Look for Plasmodium parasites.
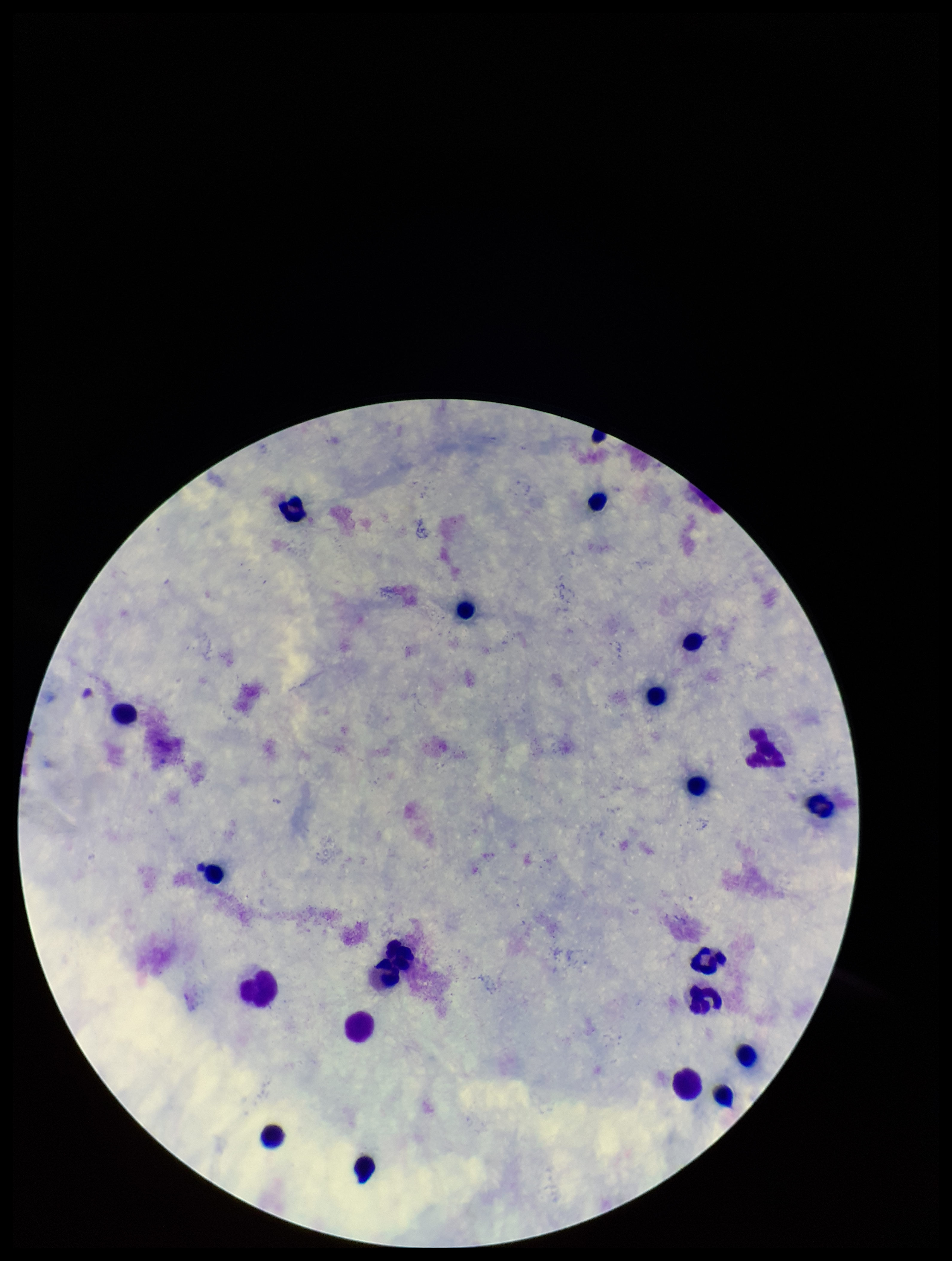

None seen.

Summary:
  - Patient malaria status: negative
  - Leukocyte count: 19
  - Capture: smartphone photograph through the microscope eyepiece
  - Preparation: thick blood smear
  - Field of view: single
  - Stain: Giemsa
  - Parasite count: 0
  - Image size: 952×1261 pixels